Assess the morphology of the red blood cells.
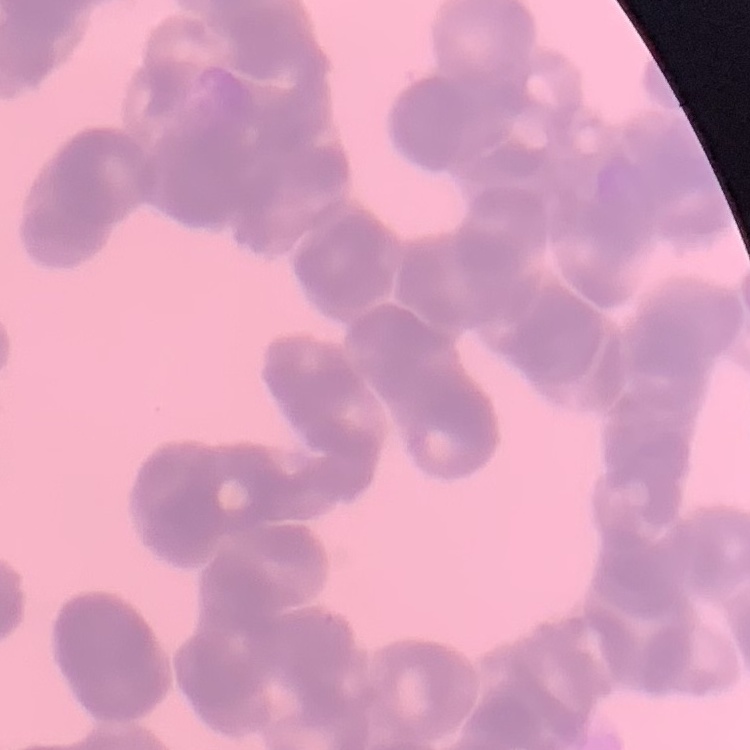
Rouleaux formation.

Field's or Giemsa stain. Square crop of a larger photomicrograph. Thin blood smear.